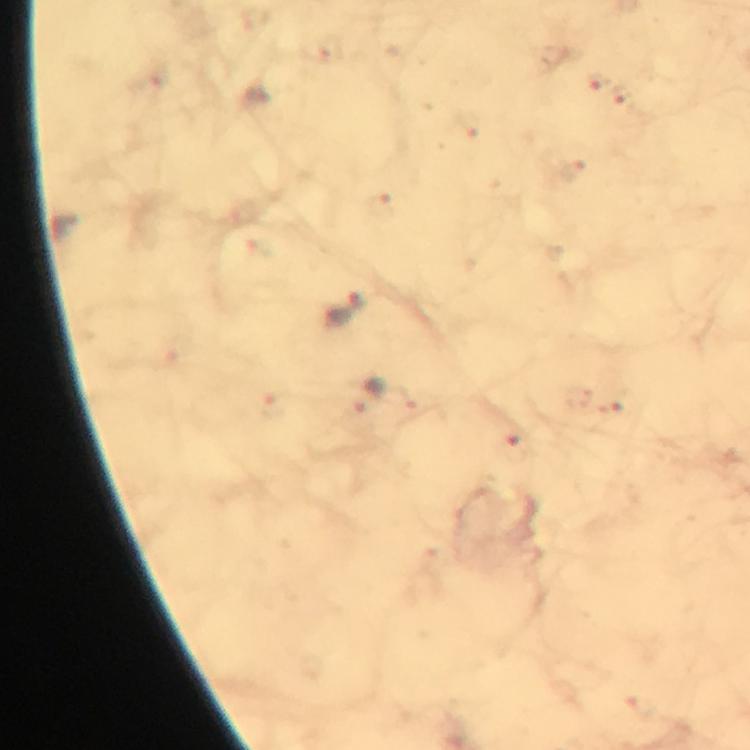

{
  "immersion_oil": "used",
  "capture": "smartphone mounted on the microscope",
  "magnification": "100x",
  "cropped_from": "a single field of view",
  "context": "from a malaria diagnostic workup",
  "preparation": "thick blood smear",
  "image_size": "750×750 pixels",
  "stain": "Giemsa",
  "malaria_parasite_locations": "approximate object centers, in pixels from the top-left corner: (x=346, y=312)"
}